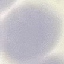
Summary:
  - Malaria status: uninfected
  - Preparation: thin blood smear
  - Image type: automatically extracted cell patch, resized to 64 × 64 pixels
  - Capture: smartphone camera at the microscope eyepiece
  - Stain: Giemsa